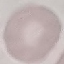 Malaria status: uninfected. Photographed with a smartphone camera at the microscope eyepiece. Cell patch, automatically extracted from a larger field of view and resized to 64 × 64 pixels. Giemsa-stained preparation. Thin blood smear.